Describe the morphology of the erythrocytes.
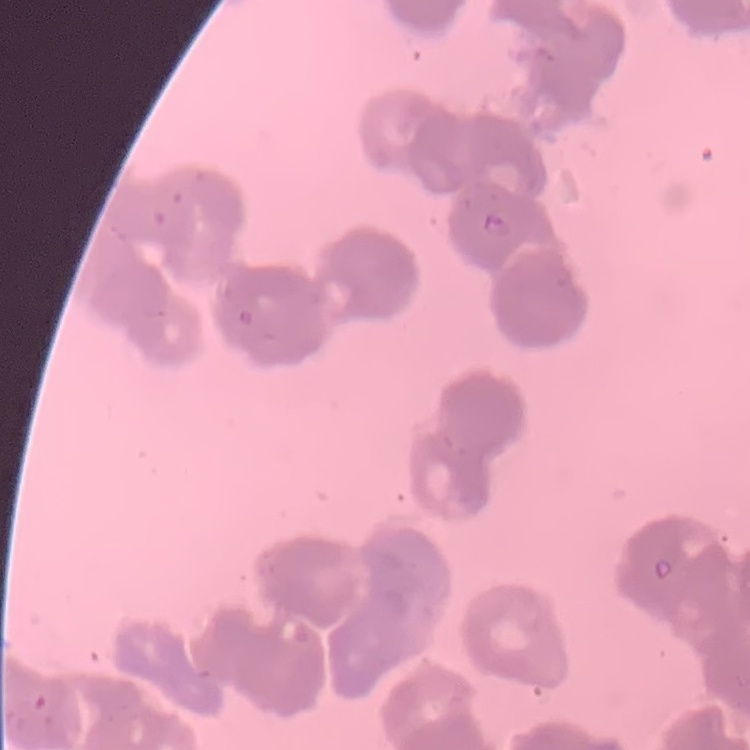

Rouleaux formation.

{
  "stain": "Field's or Giemsa",
  "image_type": "one tile cut from a larger photomicrograph",
  "preparation": "thin blood smear"
}